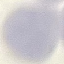

malaria status = uninfected
capture = smartphone camera at the microscope eyepiece
preparation = thin smear
image type = automatically extracted cell patch, resized to 64 × 64 pixels
stain = Giemsa